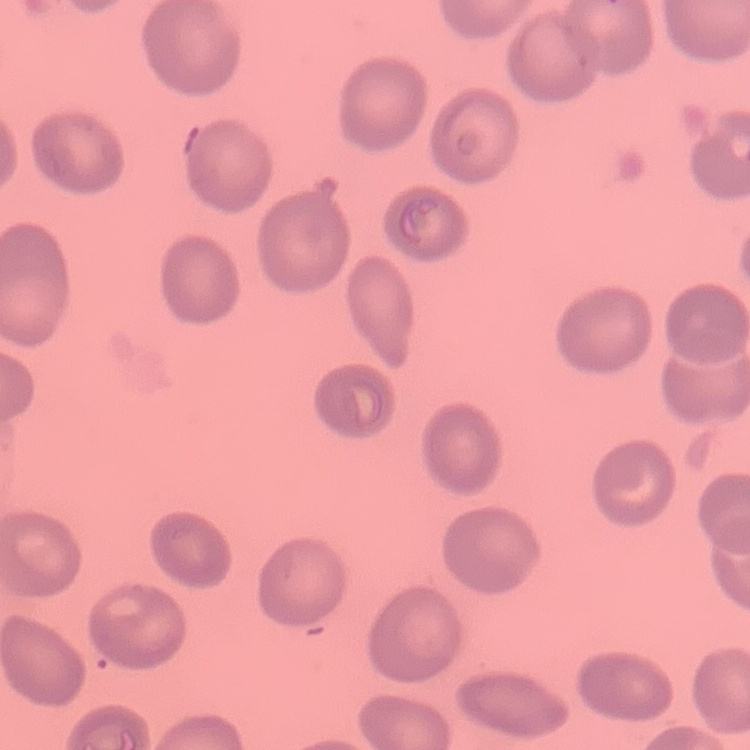
red blood cell morphology = no rouleaux formation
image type = one tile cut from a larger photomicrograph
stain = Field's or Giemsa
preparation = thin blood film